Assess this cell for malaria.
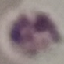
Uninfected.

Summary:
  - Stain: Giemsa
  - Capture: smartphone through the microscope eyepiece
  - Image type: automatically extracted cell patch, resized to 64 × 64 pixels
  - Preparation: thin blood smear